Classify this cell by malaria status.
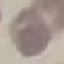

It is uninfected.

capture = smartphone camera at the microscope eyepiece
stain = Giemsa
image type = automatically extracted cell patch, resized to 64 × 64 pixels
preparation = thin blood film